Locate every leukocyte (white blood cell).
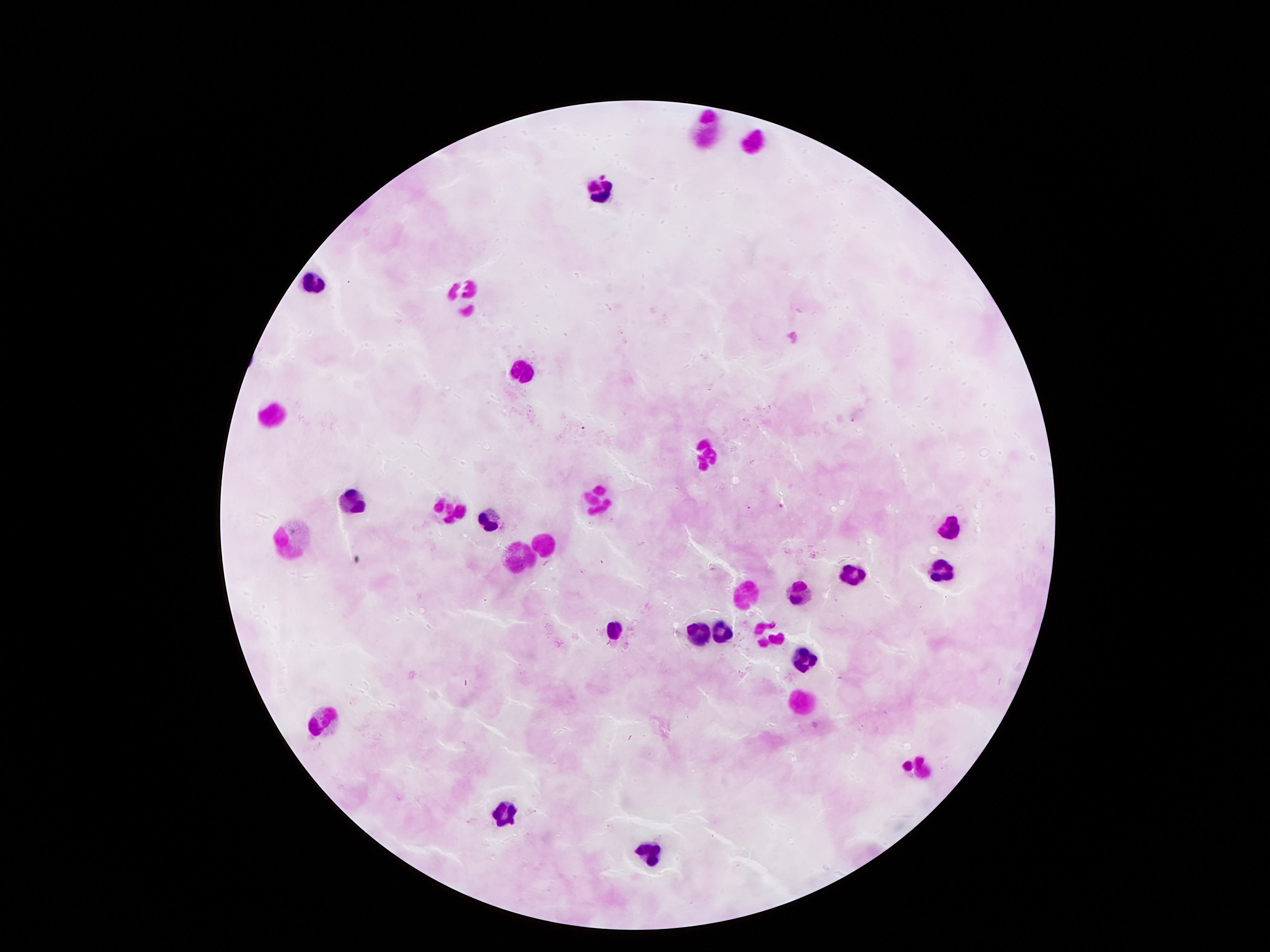

Approximate centers as [x, y] in pixels.
Leukocytes: [703, 132], [752, 143], [597, 192], [315, 282], [467, 294], [519, 370], [271, 413], [701, 452], [594, 496], [354, 500], [452, 508], [485, 518], [956, 525], [288, 537], [544, 542], [515, 557], [854, 570], [939, 572], [796, 592], [748, 599], [728, 627], [612, 629], [769, 629], [696, 633], [803, 661], [801, 700], [325, 718], [917, 774], [504, 813], [648, 846].

image size = 1270×952 pixels
stain = Giemsa
capture = smartphone camera through the microscope eyepiece
field of view = one from this slide
patient malaria status = not infected
magnification = 100x
preparation = thick blood smear